Name the parasite shown.
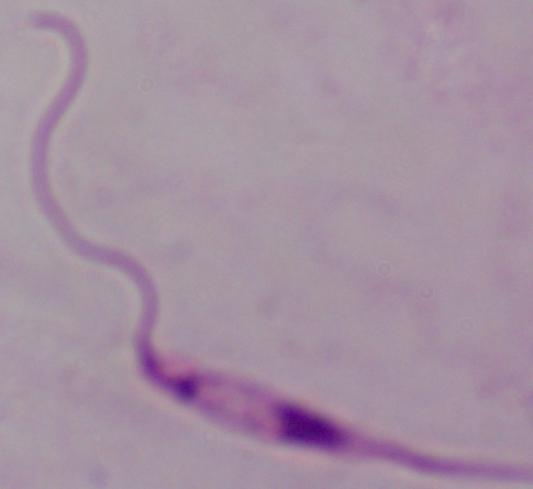

Leishmania.

magnification: 1000x
modality: photomicrograph